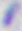

Summary:
  - Identification: Toxoplasma gondii
  - Magnification: 400x
  - Modality: photomicrograph